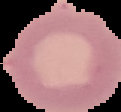 From a thin blood film. Malaria status: uninfected. Cell region segmented out of the field of view; the surrounding area is masked to black. Image is 121×112 pixels.